State which cell type is depicted.
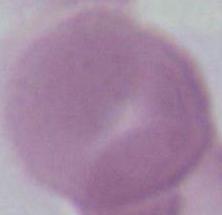

This is an erythrocyte.

{
  "magnification": "1000x",
  "modality": "photomicrograph"
}